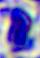 400x magnification. A white blood cell is shown. Micrograph.